Assess the morphology of the red blood cells.
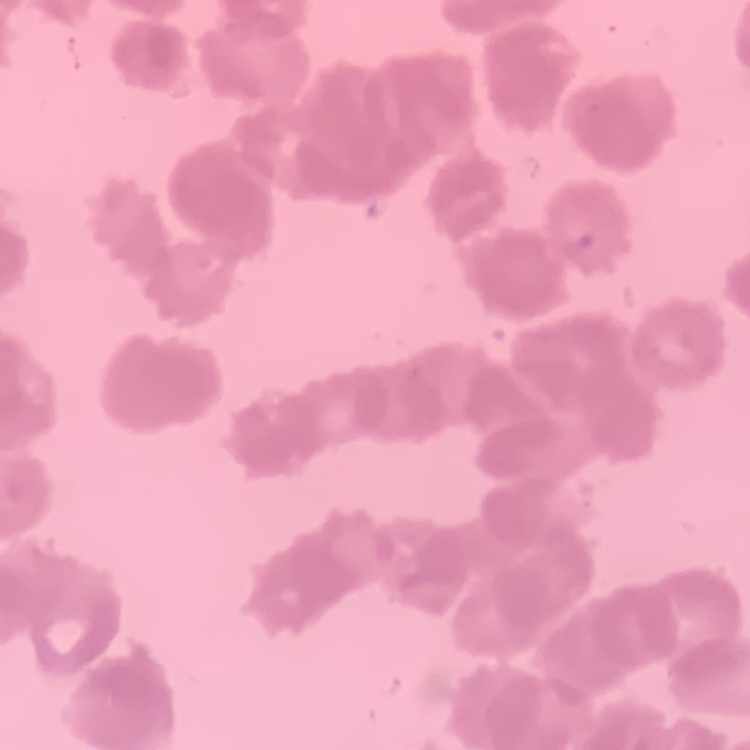
They show rouleaux formation.

Summary:
  - Stain: Field's or Giemsa
  - Preparation: thin blood film
  - Image type: one tile cut from a larger photomicrograph